Assess this cell for malaria.
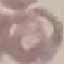
It is uninfected.

Thin blood smear. Automatically extracted cell patch, resized to 64 × 64 pixels. Photographed with a smartphone camera at the microscope eyepiece. Giemsa stain.